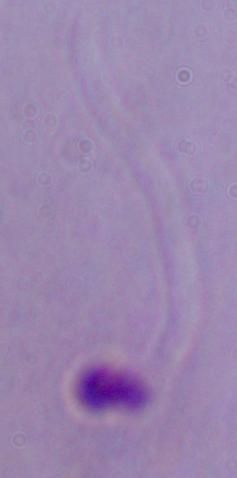

Captured at 1000x magnification. A Leishmania parasite is seen. Photomicrograph.